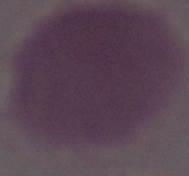

Captured at 1000x magnification. Photomicrograph. An erythrocyte is shown.